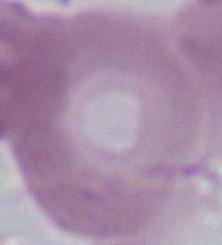

identification = red blood cell
modality = micrograph
magnification = 1000x